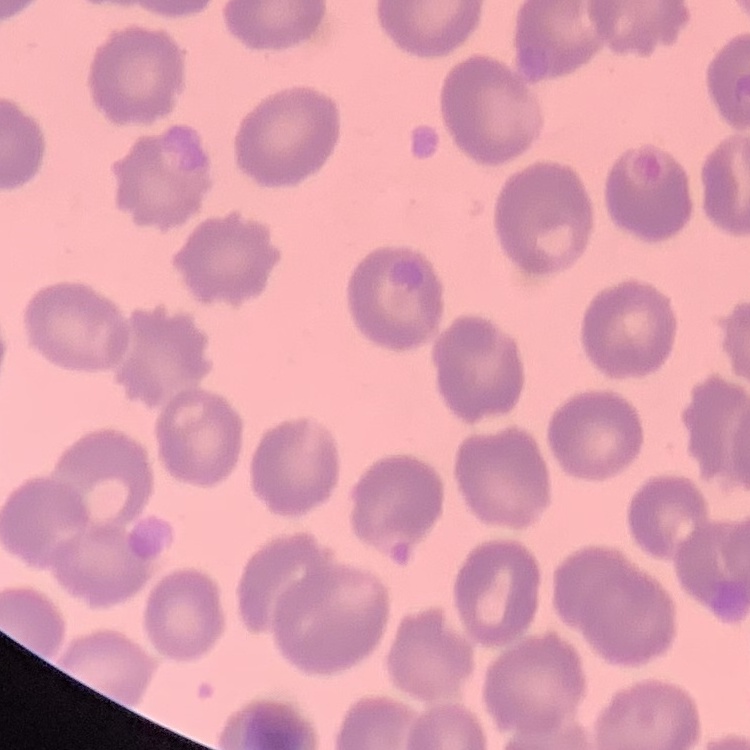 The red blood cells show no rouleaux formation. Field's or Giemsa stain. One tile cut from a larger photomicrograph. Thin blood smear.